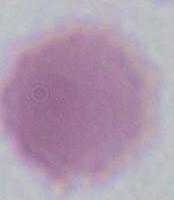

Summary:
  - Identification: red blood cell
  - Magnification: 1000x
  - Modality: photomicrograph